Name the cell type shown.
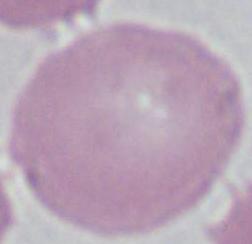

An erythrocyte.

1000x magnification. Micrograph.